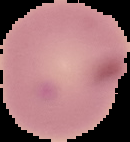
Summary:
  - Image size: 130×142 pixels
  - Preparation: thin blood film
  - Image type: cell region segmented out of the field of view; surrounding area masked to black
  - Malaria status: uninfected